Assess this cell for malaria.
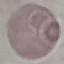
Uninfected.

Summary:
  - Stain: Giemsa
  - Capture: smartphone camera at the microscope eyepiece
  - Image type: cell patch, automatically extracted from a larger field of view and resized to 64 × 64 pixels
  - Preparation: thin smear